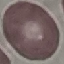

{
  "result": "negative for malaria parasites",
  "image_type": "cell patch, automatically extracted from a larger field of view and resized to 64 × 64 pixels",
  "capture": "smartphone camera at the microscope eyepiece",
  "preparation": "thin blood film",
  "stain": "Giemsa"
}